Locate every Trypanosoma brucei.
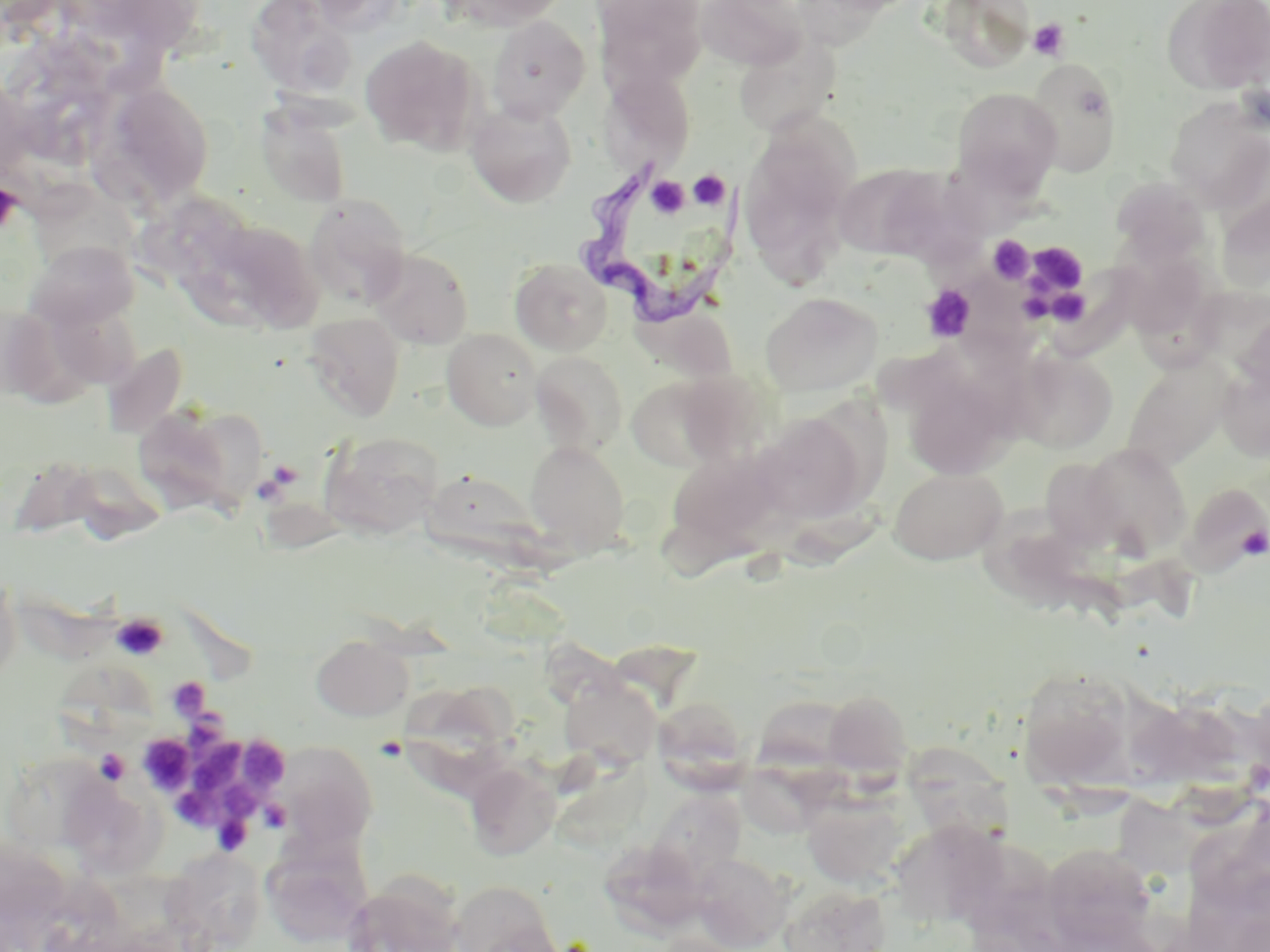
Approximate bounding boxes as [x1, y1, x2, y2] in pixels.
Trypanosoma brucei: [578, 164, 742, 329].

Uninfected red blood cell locations: [246, 0, 357, 100], [442, 0, 569, 31], [595, 0, 708, 92], [694, 0, 809, 71], [936, 0, 1036, 73], [1161, 0, 1270, 95], [487, 16, 591, 121], [733, 31, 842, 138], [359, 34, 483, 155], [1025, 58, 1124, 177], [600, 69, 697, 171], [100, 83, 215, 210], [951, 87, 1062, 196], [1165, 97, 1270, 210], [465, 101, 577, 208], [256, 104, 352, 209], [739, 119, 859, 276], [832, 163, 947, 260], [925, 169, 1034, 252], [1111, 176, 1211, 266], [42, 186, 157, 279], [1217, 188, 1269, 295], [139, 189, 265, 278], [304, 194, 411, 306], [204, 218, 324, 333], [24, 240, 139, 331], [369, 247, 474, 349], [1117, 249, 1213, 342], [510, 258, 612, 355], [956, 273, 1054, 384], [761, 292, 882, 397], [633, 306, 738, 384], [1235, 309, 1270, 403], [303, 313, 405, 420], [442, 328, 541, 430], [102, 342, 189, 438], [1011, 347, 1118, 452], [530, 352, 628, 455], [1122, 356, 1235, 472], [1217, 366, 1270, 463], [904, 370, 1019, 480], [626, 375, 729, 471], [132, 405, 247, 516], [753, 412, 869, 524], [320, 430, 444, 539], [524, 441, 629, 553], [1079, 443, 1193, 559], [664, 448, 783, 555], [1040, 456, 1127, 552], [888, 467, 1008, 565], [429, 473, 552, 577], [1178, 482, 1270, 575], [990, 505, 1123, 611], [0, 569, 23, 685], [311, 635, 413, 721], [57, 665, 162, 763], [1017, 667, 1137, 789], [559, 675, 663, 770], [408, 686, 520, 791], [823, 689, 912, 778], [651, 696, 751, 790], [275, 745, 378, 849], [904, 746, 1017, 871], [2, 752, 118, 856], [466, 763, 560, 860], [63, 771, 165, 875], [645, 789, 745, 885], [802, 794, 904, 889], [1185, 815, 1270, 911], [895, 820, 1014, 924], [263, 838, 374, 946], [1042, 844, 1161, 951], [161, 851, 267, 951], [2, 852, 88, 952], [692, 853, 790, 951], [342, 879, 465, 952], [449, 879, 564, 952], [779, 884, 891, 952], [649, 932, 746, 952]. Platelet locations: [1027, 18, 1069, 60], [688, 170, 729, 210], [643, 176, 691, 218], [0, 182, 21, 233], [988, 235, 1035, 284], [1025, 242, 1090, 297], [921, 285, 977, 342], [1238, 525, 1269, 562], [111, 613, 169, 660], [167, 677, 209, 719], [191, 709, 232, 765], [138, 734, 194, 793], [246, 737, 289, 791], [196, 743, 248, 795], [94, 748, 130, 785], [223, 780, 266, 823], [176, 788, 228, 831], [258, 800, 292, 833], [214, 814, 252, 855]. Slide-level diagnosis: Trypanosoma brucei. Single field of view. Light microscopy. Image is 1270×952 pixels. Thin blood film. May-Grünwald-Giemsa stain. Captured at 1000x magnification.